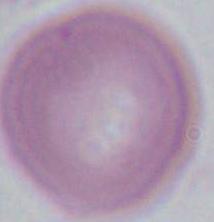

A red blood cell is seen. 1000x magnification. Micrograph.